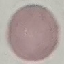 Result: no malaria parasites seen. Thin smear of blood. Cell patch, automatically extracted from a larger field of view and resized to 64 × 64 pixels. Giemsa stain. Acquired by smartphone through the microscope eyepiece.